Name the cell type shown.
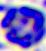

A leukocyte.

Summary:
  - Magnification: 400x
  - Modality: photomicrograph